Classify this cell by malaria status.
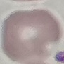
Uninfected.

Cell patch, automatically extracted from a larger field of view and resized to 64 × 64 pixels. Thin blood smear. Photographed with a smartphone camera at the microscope eyepiece. Giemsa-stained preparation.